Give the position of every leukocyte visible.
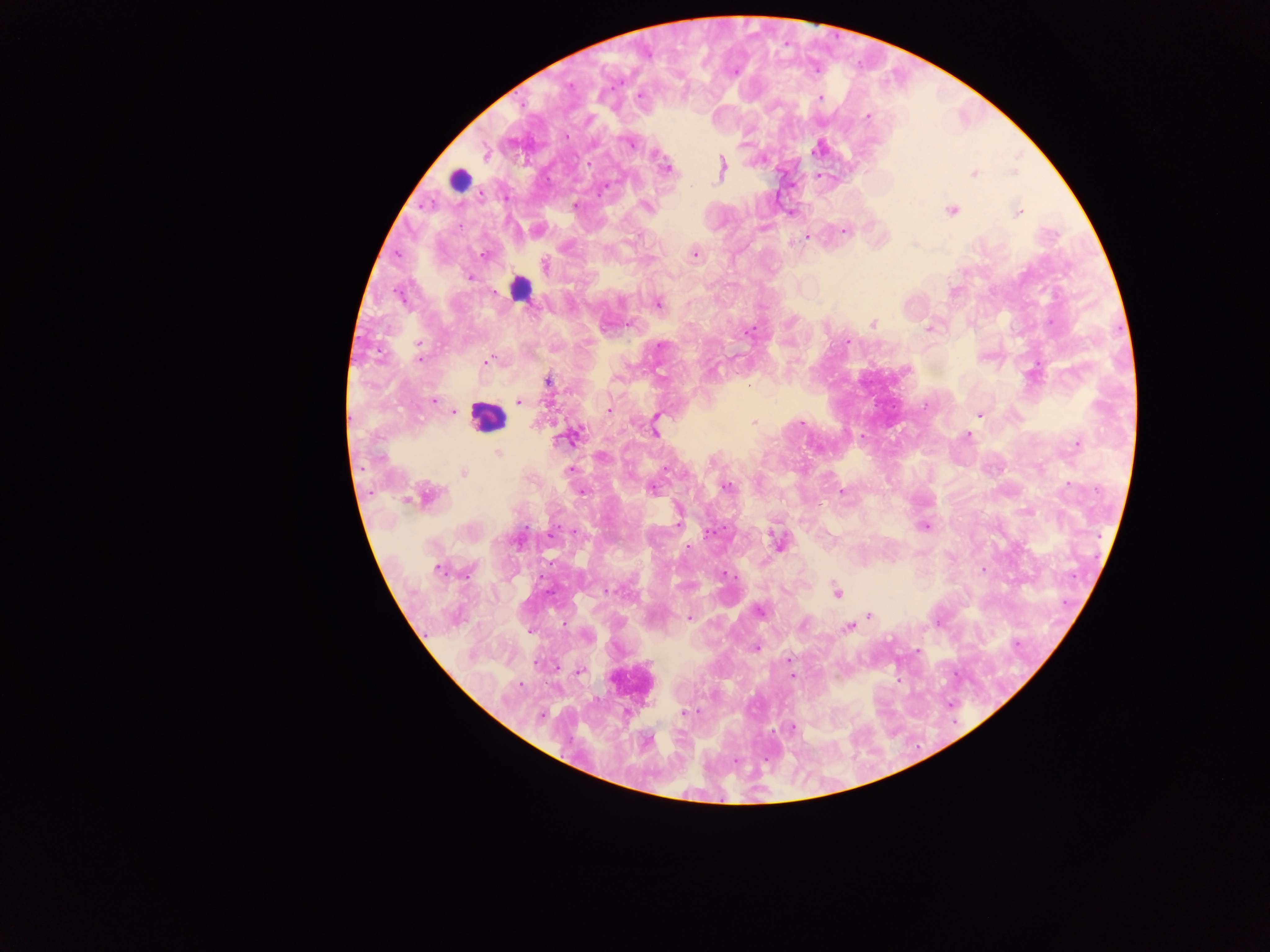
Approximate centers as (x, y) in pixels.
Leukocytes: (461, 179), (517, 286), (483, 419).

Malaria parasite locations: (734, 73), (819, 99), (867, 117), (567, 135), (746, 136), (630, 143), (816, 147), (656, 152), (721, 168), (668, 169), (973, 173), (815, 178), (607, 187), (575, 202), (647, 206), (950, 211), (1019, 212), (790, 214), (845, 233), (805, 236), (914, 245), (694, 253), (485, 256), (545, 262), (469, 277), (657, 303), (793, 323), (872, 324), (926, 328), (750, 332), (418, 346), (659, 346), (420, 360), (793, 361), (487, 362), (713, 371), (1031, 374), (548, 382), (520, 400), (432, 401), (607, 409), (454, 411), (657, 415), (979, 415), (752, 422), (801, 426), (654, 433), (574, 434), (967, 436), (1074, 442), (570, 469), (666, 471), (727, 487), (651, 489), (842, 490), (582, 492), (429, 497), (408, 501), (679, 516), (924, 528), (709, 532), (776, 543), (439, 570), (983, 571), (544, 579), (608, 591), (835, 592), (868, 615), (688, 616), (849, 628), (528, 629), (756, 647), (790, 659), (580, 670), (896, 679), (518, 686), (686, 711). Thick blood smear. Collected in Ghana. Image is 1270×952 pixels. Mobile-phone photograph taken through the microscope. Single field of view.